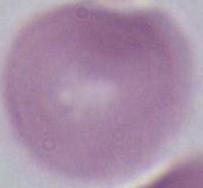
identification: erythrocyte
magnification: 1000x
modality: micrograph